Identify the parasite.
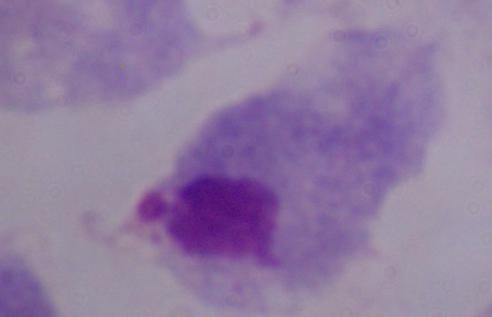

This is a trichomonad.

Summary:
  - Magnification: 1000x
  - Modality: photomicrograph